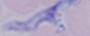
identification = trypanosome
modality = photomicrograph
magnification = 1000x